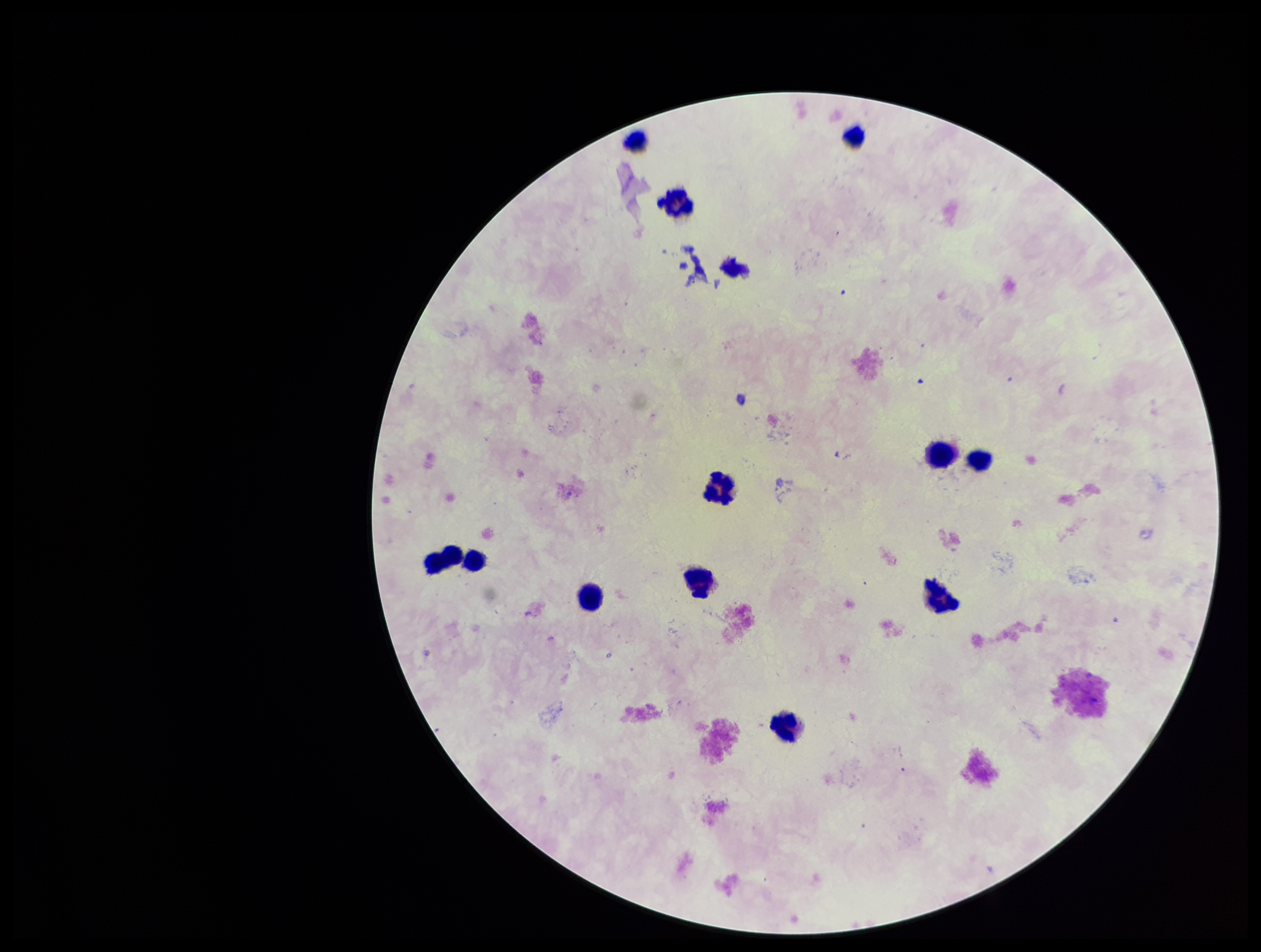

capture: smartphone photograph through the microscope eyepiece
parasite_count: 0
leukocyte_count: 13
stain: Giemsa
plasmodium_parasites: none identified
field_of_view: single
patient_malaria_status: negative
preparation: thick smear
image_size: 1261×952 pixels